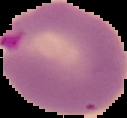

Summary:
  - Image type: segmented cell region with the area outside set to black
  - Image size: 127×118 pixels
  - Preparation: thin blood smear
  - Malaria status: parasitized